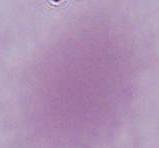
identification = erythrocyte
modality = photomicrograph
magnification = 1000x